Assess the morphology of the red blood cells.
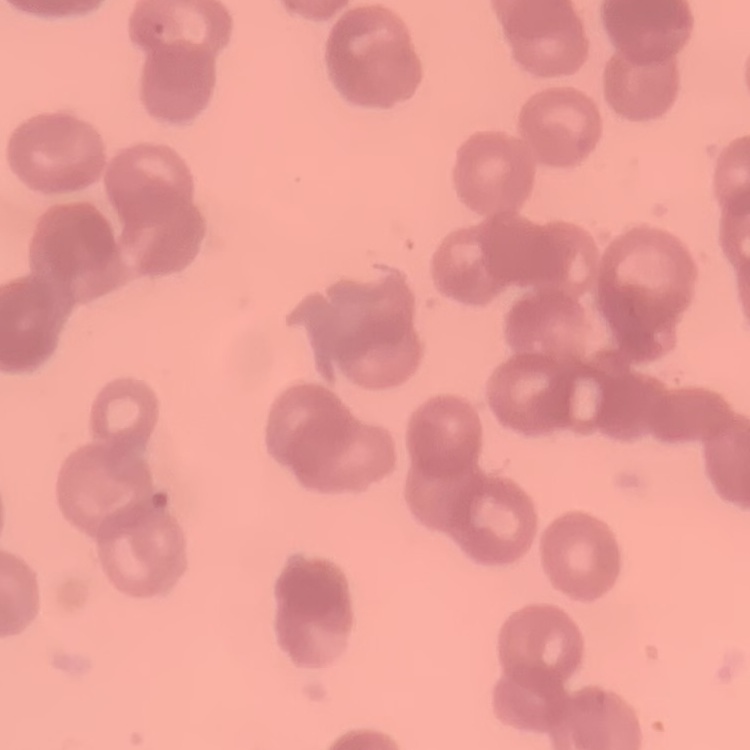
They show rouleaux formation.

Summary:
  - Stain: Field's or Giemsa
  - Image type: square crop of a larger photomicrograph
  - Preparation: thin blood smear